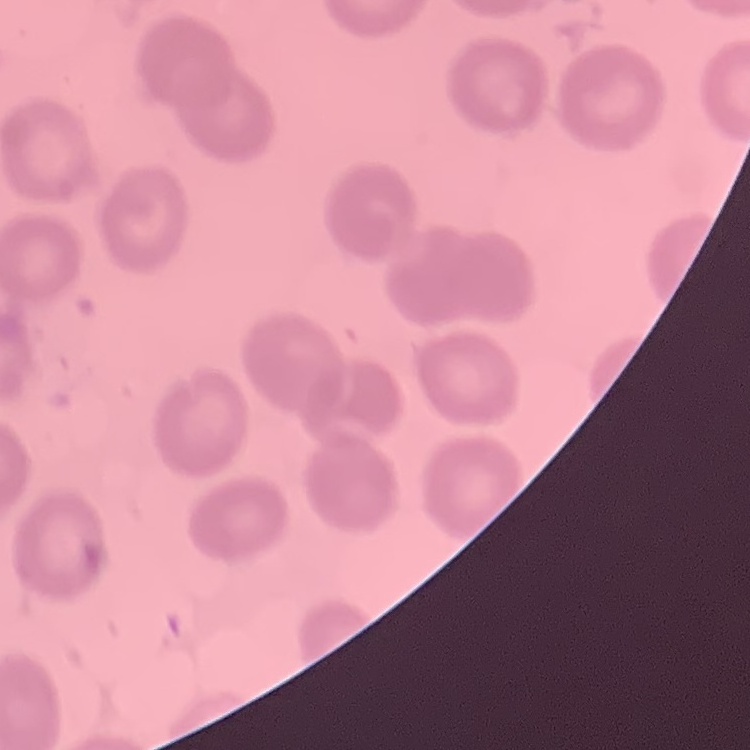
Summary:
  - Red blood cell morphology: no rouleaux formation
  - Image type: square crop of a larger photomicrograph
  - Preparation: thin blood smear
  - Stain: Field's or Giemsa